Assess this cell for malaria.
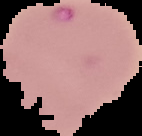

It is parasitized.

Summary:
  - Preparation: thin blood film
  - Image size: 142×136 pixels
  - Image type: segmented cell region on a black background